Comment on the morphology of the erythrocytes.
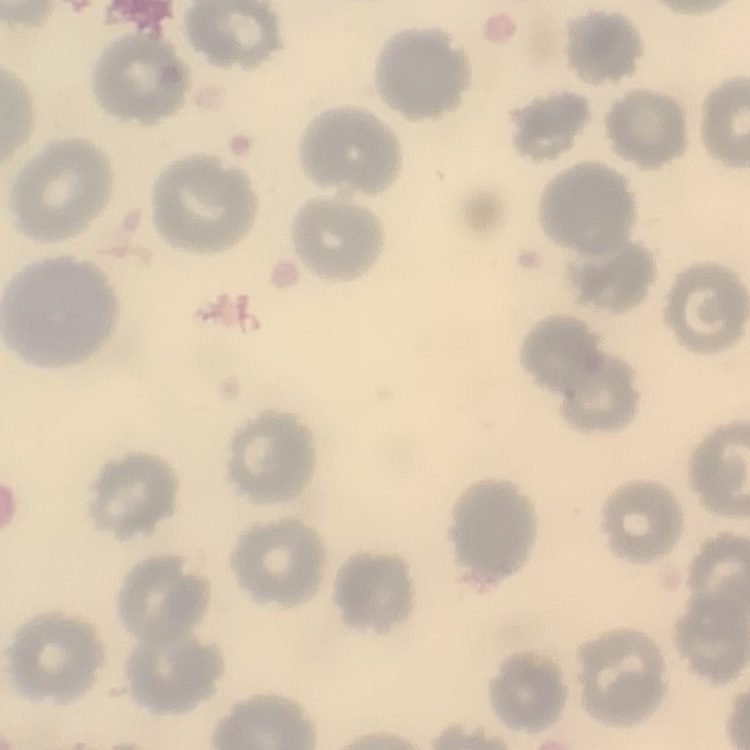

No rouleaux formation.

Thin blood smear. One tile cut from a larger photomicrograph. Stained with either Field's or Giemsa.